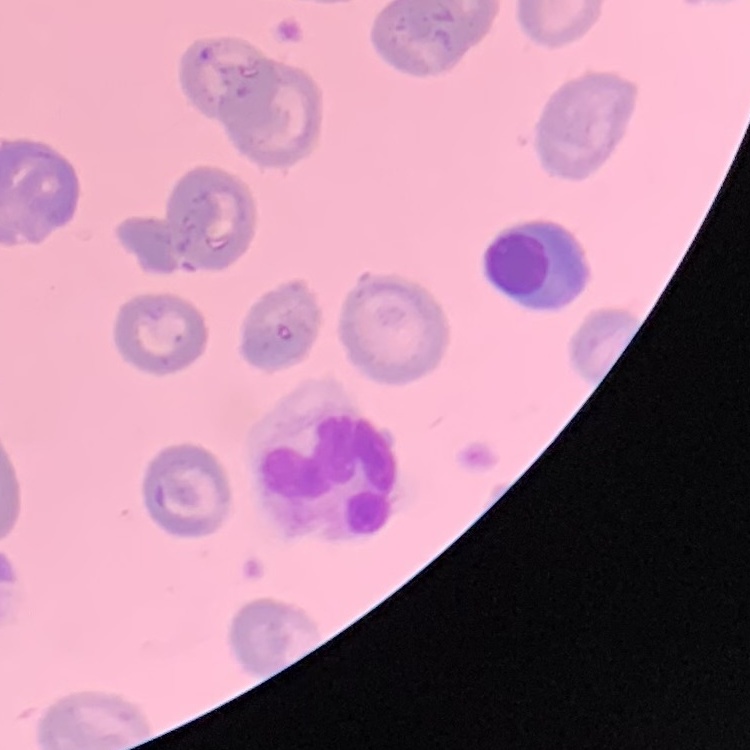
Summary:
  - Red blood cell morphology: no rouleaux formation
  - Image type: one tile cut from a larger photomicrograph
  - Preparation: thin peripheral smear
  - Stain: Field's or Giemsa